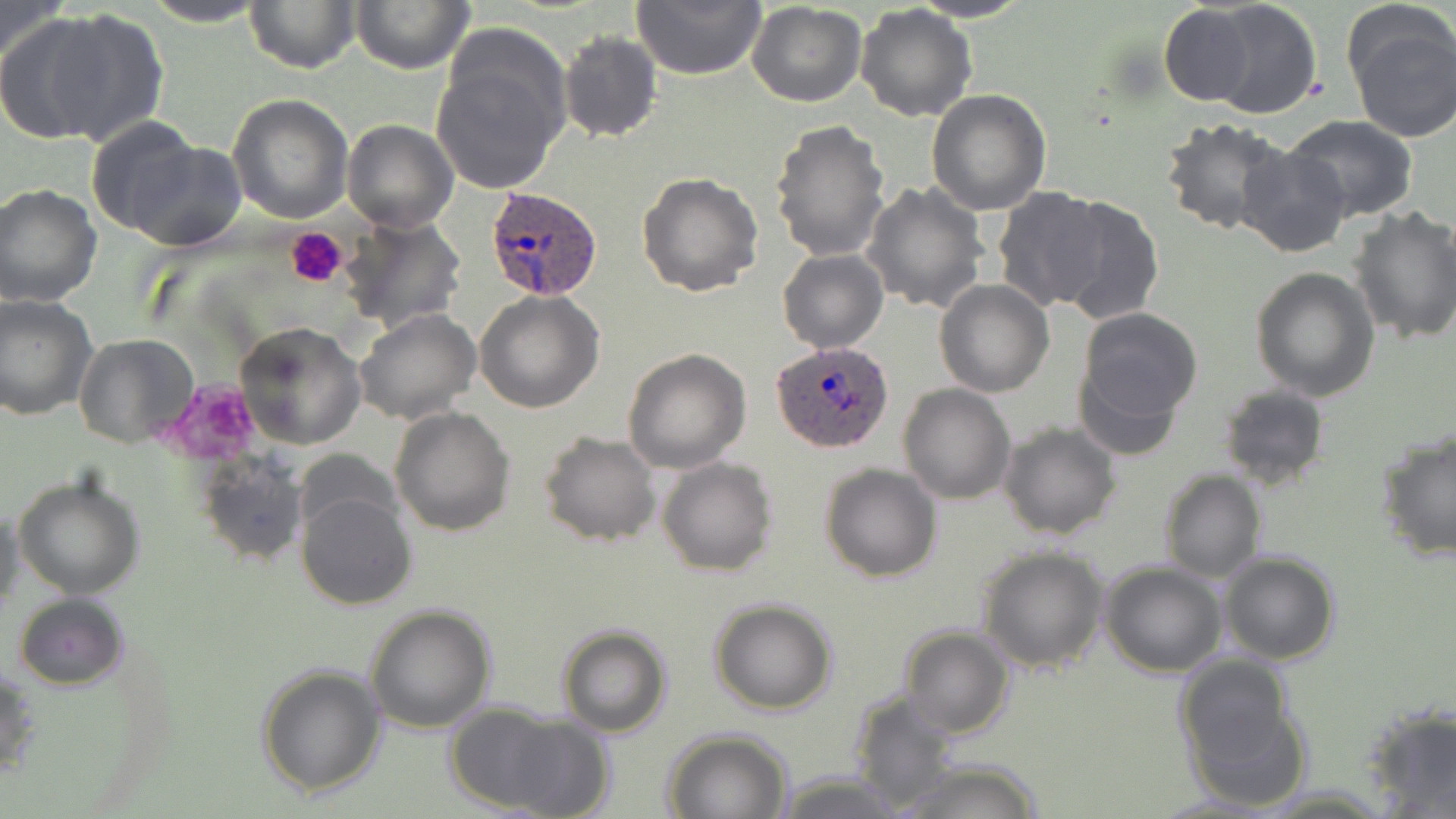

Summary:
  - Coordinate format: approximate bounding boxes as (x1,y1)-(x2,y2) corner pairs in pixels
  - Platelet locations: (285,227)-(347,289), (164,381)-(267,465)
  - Uninfected red blood cell locations: (244,0)-(360,74), (633,0)-(767,81), (907,0)-(1034,23), (1207,0)-(1323,119), (141,1)-(272,26), (0,2)-(68,68), (351,2)-(474,74), (747,2)-(867,107), (1157,4)-(1255,106), (855,5)-(978,122), (39,10)-(168,146), (0,12)-(112,142), (1347,14)-(1456,143), (432,29)-(571,196), (558,31)-(662,144), (926,89)-(1052,214), (226,94)-(354,224), (1284,114)-(1419,221), (82,117)-(206,238), (341,117)-(459,233), (1159,117)-(1291,236), (770,119)-(890,261), (119,135)-(249,250), (1236,145)-(1355,258), (638,171)-(765,298), (861,182)-(988,314), (0,183)-(103,307), (992,185)-(1106,313), (1052,194)-(1164,325), (1348,206)-(1456,344), (338,214)-(467,334), (777,249)-(887,353), (1250,265)-(1380,402), (934,280)-(1054,398), (475,290)-(605,411), (0,292)-(98,419), (1076,308)-(1203,430), (354,309)-(480,425), (234,321)-(365,450), (74,334)-(199,448), (622,348)-(752,475), (898,383)-(1016,503), (1217,384)-(1329,490), (390,406)-(515,536), (998,421)-(1122,539), (1376,429)-(1456,564), (539,431)-(662,546), (198,455)-(309,568), (658,456)-(777,576), (820,463)-(942,583), (1159,469)-(1267,582), (12,470)-(146,599), (295,489)-(417,610), (1,502)-(25,614), (977,545)-(1109,671), (1219,550)-(1340,663), (1100,563)-(1228,678), (12,593)-(129,691), (708,599)-(837,715), (364,605)-(496,733), (556,624)-(670,737), (899,625)-(1014,739), (1,661)-(37,786), (255,663)-(387,797), (1176,665)-(1303,808), (846,691)-(962,810), (440,702)-(591,817), (1361,705)-(1456,816), (658,729)-(794,819), (888,759)-(1048,819), (771,773)-(917,818)
  - Plasmodium ovale-infected red blood cell locations: (483,186)-(605,301), (769,341)-(895,454)
  - Slide-level diagnosis: Plasmodium ovale
  - Field of view: one of a larger specimen
  - Magnification: 1000x
  - Stain: May-Grünwald-Giemsa
  - Image size: 1456×819 pixels
  - Preparation: thin blood film
  - Modality: light microscopy